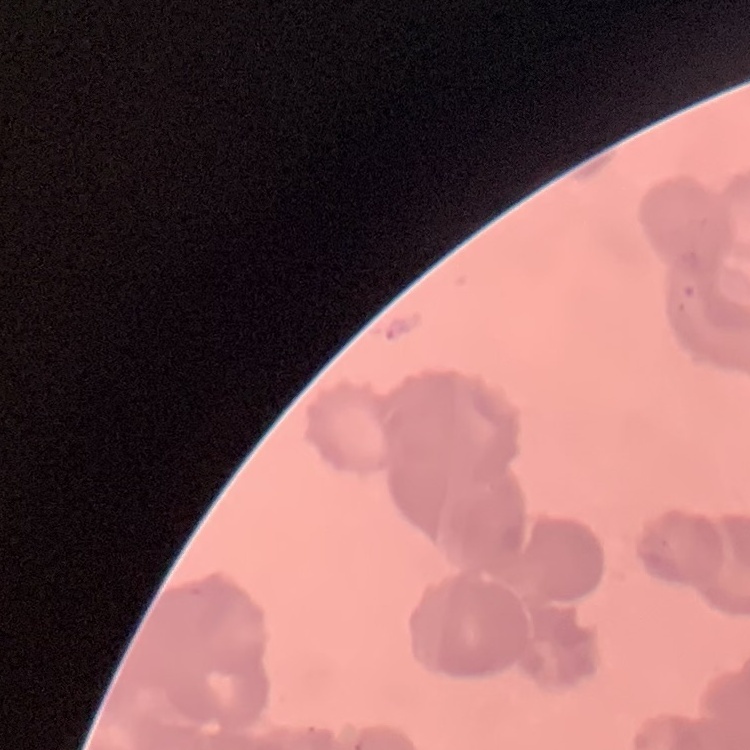
The erythrocytes exhibit rouleaux formation. One tile cut from a larger photomicrograph. Stained with either Field's or Giemsa. Thin blood film.